Locate every Plasmodium parasite.
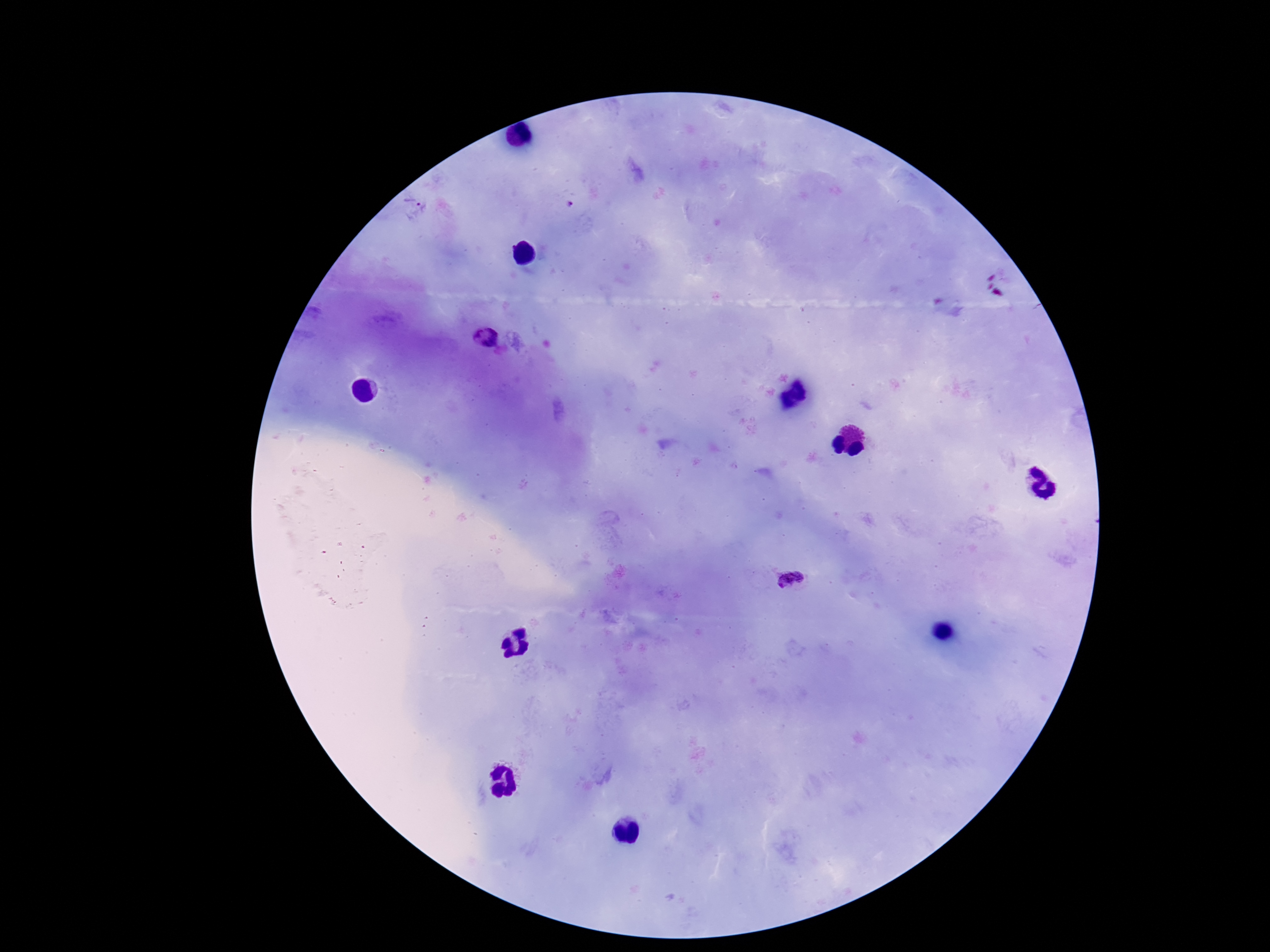

Approximate centers as (x, y) in pixels.
Plasmodium parasites: (483, 340), (795, 579).

{
  "patient_malaria_status": "positive",
  "field_of_view": "one from this slide",
  "capture": "smartphone camera through the microscope eyepiece",
  "image_size": "1270×952 pixels",
  "stain": "Giemsa",
  "preparation": "thick peripheral-blood smear",
  "magnification": "100x"
}